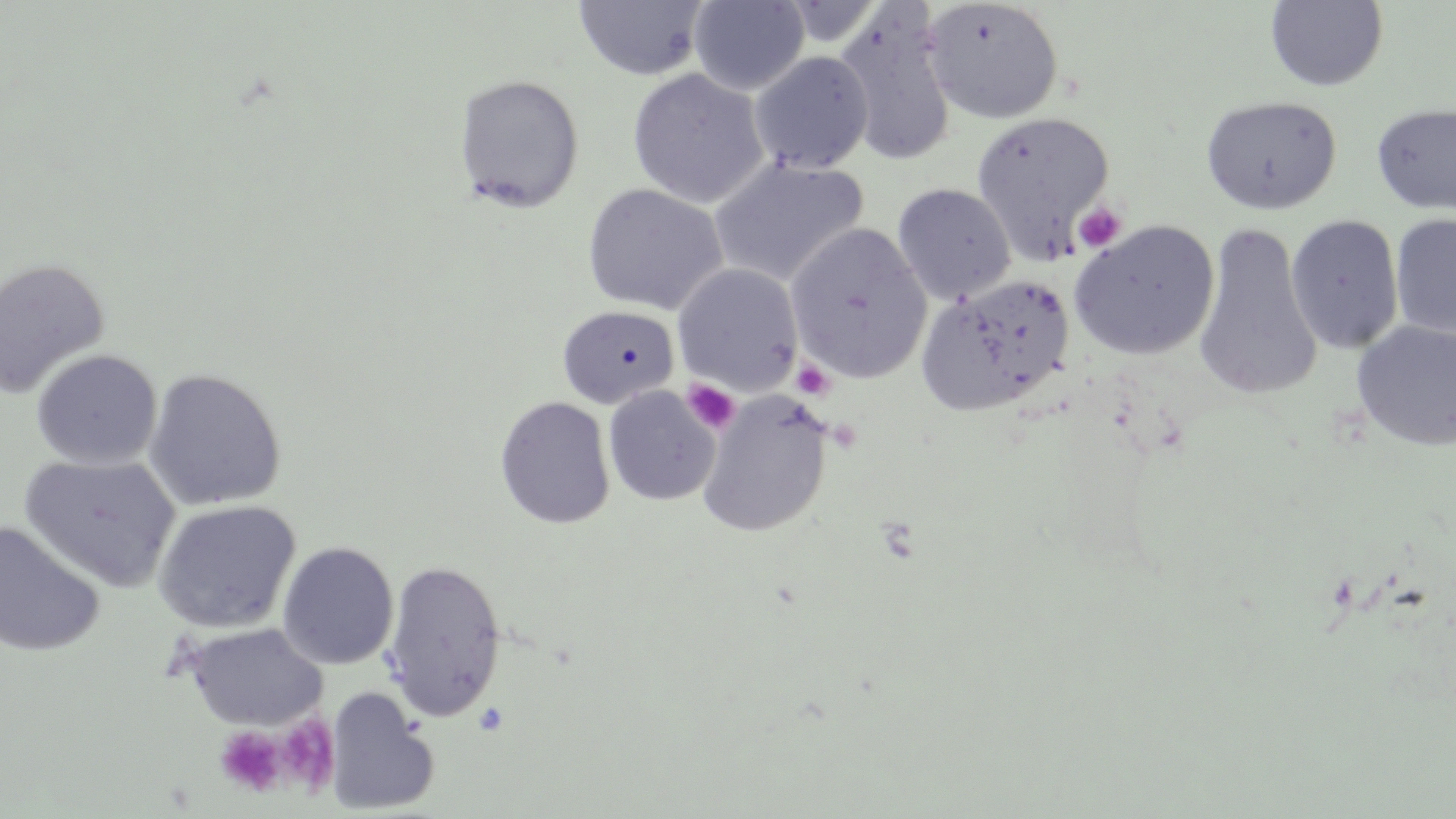

{
  "slide_level_diagnosis": "no evidence of blood parasites",
  "field_of_view": "single",
  "stain": "May-Grünwald-Giemsa",
  "magnification": "1000x",
  "modality": "optical microscopy",
  "image_size": "1456×819 pixels",
  "preparation": "thin blood smear",
  "platelet_locations": "approximate bounding boxes as [x1, y1, x2, y2] in pixels: [1072, 201, 1128, 254], [791, 359, 835, 401], [681, 379, 741, 435], [275, 715, 340, 794], [215, 726, 287, 797]",
  "uninfected_red_blood_cell_locations": "approximate bounding boxes as [x1, y1, x2, y2] in pixels: [1265, 0, 1389, 92], [572, 1, 710, 80], [688, 1, 810, 95], [921, 1, 1064, 124], [834, 7, 958, 168], [749, 51, 874, 174], [626, 68, 769, 208], [453, 73, 586, 213], [1200, 95, 1342, 215], [1371, 102, 1456, 216], [970, 112, 1116, 262], [709, 157, 869, 288], [582, 183, 728, 316], [891, 183, 1017, 306], [1390, 212, 1456, 342], [1285, 214, 1404, 354], [1069, 220, 1220, 361], [787, 222, 931, 384], [1193, 222, 1323, 402], [0, 258, 111, 399], [673, 263, 802, 395], [916, 274, 1075, 416], [556, 305, 681, 410], [1351, 321, 1456, 452], [31, 349, 162, 469], [144, 367, 287, 511], [603, 386, 720, 506], [696, 394, 831, 538], [494, 395, 615, 529], [19, 453, 181, 593], [152, 500, 301, 633], [0, 521, 106, 657], [277, 541, 399, 670], [381, 558, 507, 722], [182, 622, 326, 730], [323, 687, 440, 815]"
}